Identify the cell.
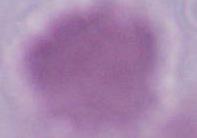
An erythrocyte.

Summary:
  - Magnification: 1000x
  - Modality: photomicrograph